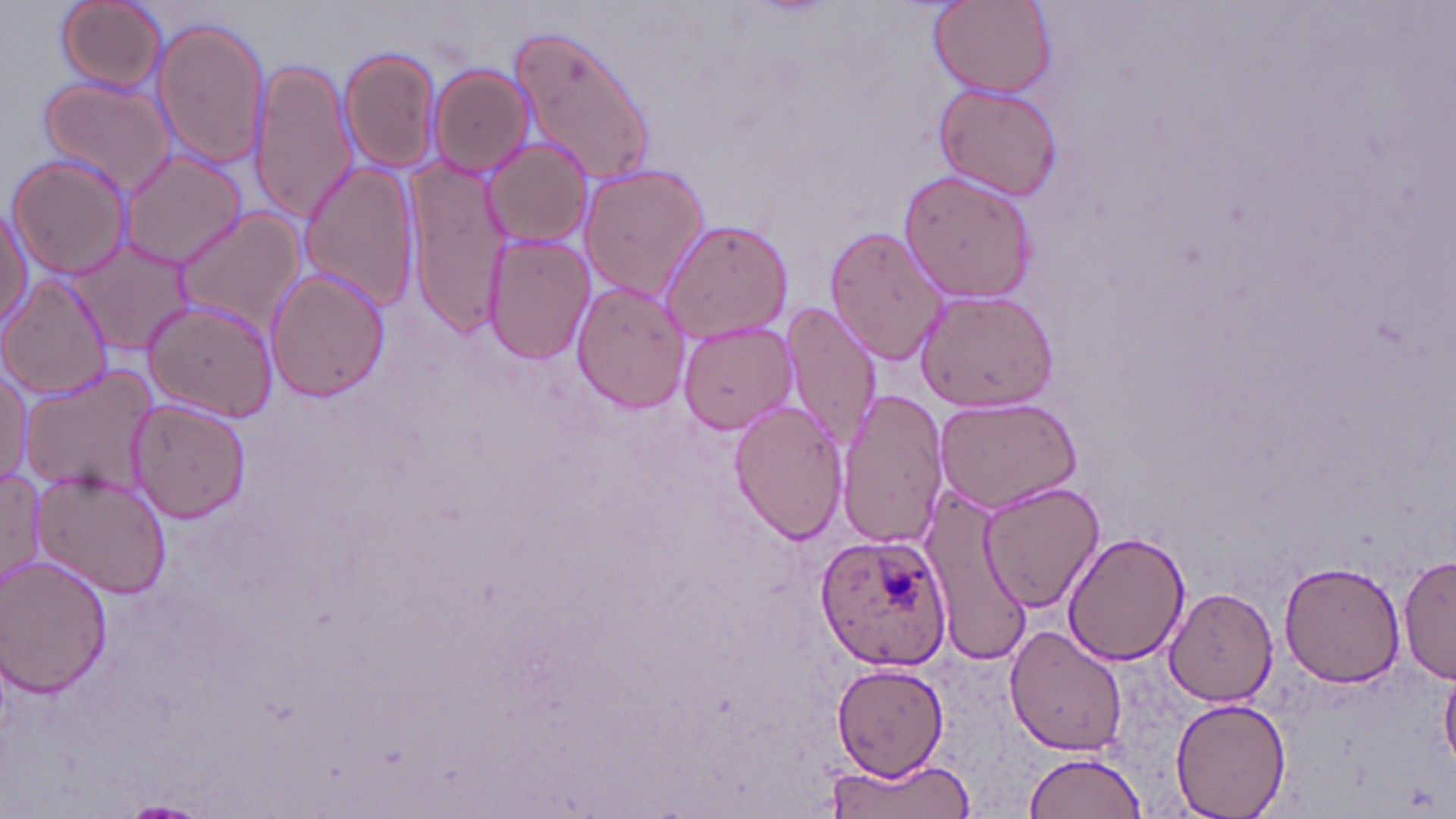

slide-level diagnosis = Plasmodium ovale
stain = May-Grünwald-Giemsa
field of view = single
image size = 1456×819 pixels
Plasmodium ovale-infected red blood cell locations = approximate bounding boxes as [x1, y1, x2, y2] in pixels: [815, 533, 955, 671]
preparation = thin blood smear
modality = optical microscopy
uninfected red blood cell locations = approximate bounding boxes as [x1, y1, x2, y2] in pixels: [52, 0, 170, 95], [928, 0, 1055, 99], [151, 18, 270, 171], [509, 24, 657, 189], [337, 45, 443, 175], [245, 59, 358, 225], [429, 64, 533, 179], [39, 77, 176, 198], [933, 81, 1063, 201], [480, 138, 595, 249], [117, 149, 246, 268], [6, 153, 131, 279], [296, 160, 421, 315], [407, 162, 513, 336], [578, 164, 710, 301], [897, 168, 1038, 300], [0, 202, 32, 334], [172, 210, 305, 337], [656, 217, 793, 346], [825, 225, 951, 364], [483, 233, 597, 365], [69, 235, 201, 354], [266, 271, 388, 404], [0, 274, 113, 401], [572, 279, 692, 411], [913, 288, 1061, 412], [145, 300, 282, 424], [781, 303, 881, 453], [678, 319, 799, 433], [20, 363, 160, 497], [0, 364, 32, 486], [835, 389, 954, 550], [933, 393, 1083, 512], [729, 397, 849, 543], [127, 398, 253, 524], [30, 468, 174, 599], [0, 470, 45, 595], [979, 480, 1108, 613], [923, 489, 1029, 662], [1061, 531, 1188, 665], [1401, 556, 1456, 687], [1, 558, 113, 696], [1278, 562, 1404, 687], [1164, 586, 1279, 708], [1003, 624, 1128, 755], [832, 664, 948, 780], [1440, 672, 1456, 769], [1170, 699, 1291, 818], [1023, 751, 1148, 819], [823, 756, 979, 819]
magnification = 1000x